Assess this cell for malaria.
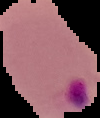

Parasitized.

Cell region segmented out of the field of view; the surrounding area is masked to black. From a thin blood film. Image is 100×118 pixels.